Locate every Babesia divergens-infected red blood cell.
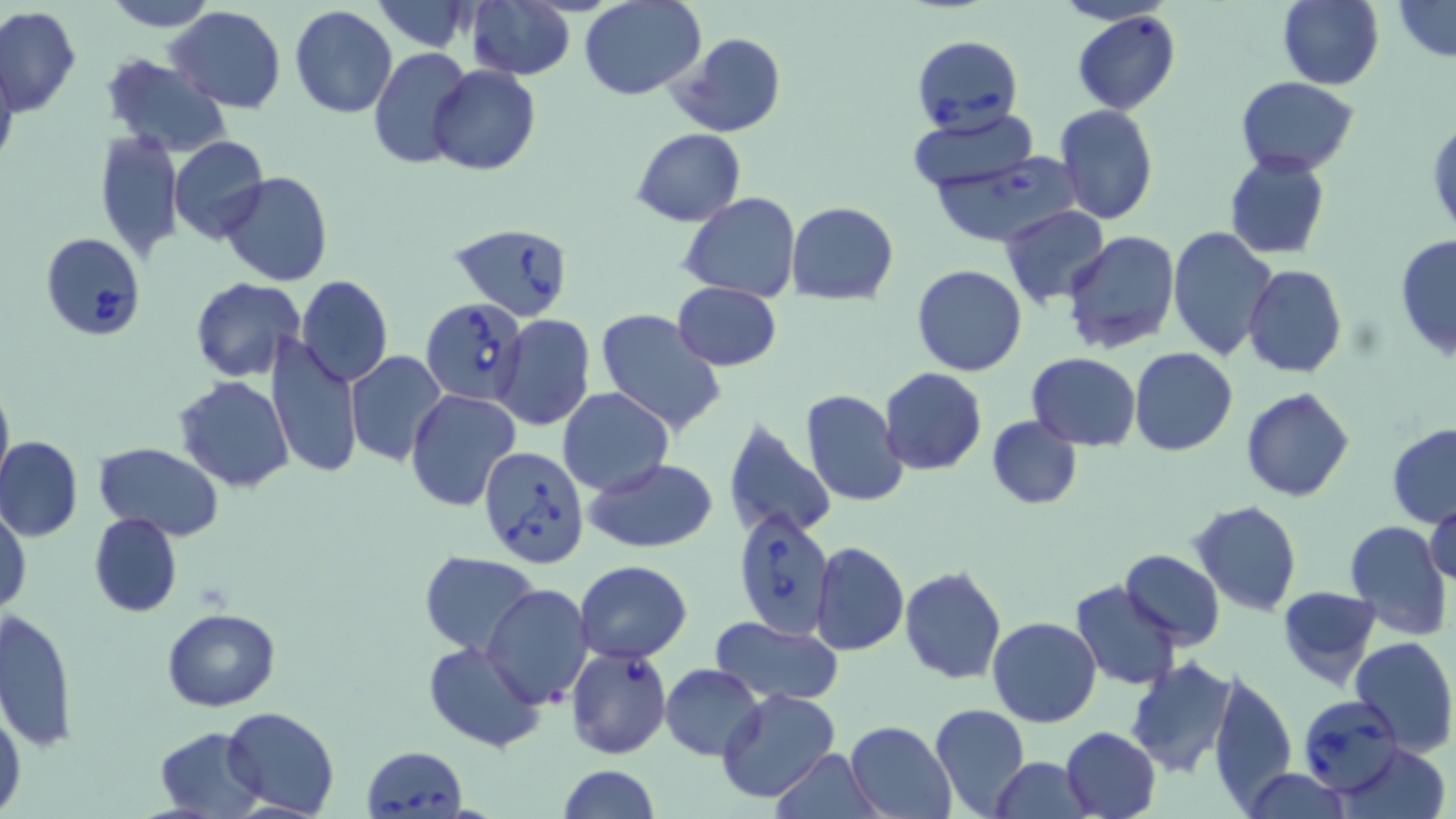

Approximate bounding boxes as (x1,y1)-(x2,y2) corner pairs in pixels.
Babesia divergens-infected red blood cells: (915,35)-(1021,134), (929,151)-(1086,248), (449,228)-(568,320), (42,234)-(148,343), (420,299)-(526,405), (478,445)-(590,569), (729,507)-(838,639), (565,646)-(672,759), (1298,694)-(1402,796), (360,746)-(467,819).

Summary:
  - Uninfected red blood cell locations: (102,0)-(218,31), (1277,0)-(1383,90), (1392,0)-(1456,62), (370,1)-(478,51), (577,1)-(707,101), (468,3)-(575,79), (289,4)-(398,119), (0,5)-(81,116), (168,7)-(287,112), (1071,11)-(1180,115), (665,31)-(789,138), (370,46)-(475,171), (104,54)-(232,157), (0,55)-(20,173), (429,66)-(540,177), (1236,75)-(1359,176), (1054,103)-(1158,224), (909,111)-(1040,191), (1428,119)-(1456,238), (631,128)-(745,226), (95,131)-(183,262), (169,135)-(269,242), (1224,149)-(1331,259), (220,170)-(332,287), (680,193)-(801,302), (785,202)-(899,304), (998,203)-(1111,307), (1169,225)-(1279,362), (1063,230)-(1179,354), (1394,234)-(1456,361), (912,264)-(1027,377), (1243,264)-(1347,380), (297,275)-(393,388), (190,277)-(304,382), (672,281)-(782,370), (596,308)-(728,437), (493,314)-(594,431), (266,334)-(363,482), (1129,346)-(1238,456), (344,351)-(449,467), (1028,351)-(1141,451), (878,367)-(987,476), (175,376)-(293,493), (0,379)-(13,491), (1240,386)-(1356,503), (557,387)-(673,497), (799,389)-(909,506), (407,390)-(522,513), (986,416)-(1081,509), (723,418)-(835,540), (1387,423)-(1456,526), (0,436)-(83,541), (95,442)-(222,541), (583,458)-(718,553), (1426,496)-(1456,592), (1190,501)-(1302,617), (0,506)-(29,618), (89,512)-(184,617), (1343,518)-(1452,639), (810,541)-(908,656), (1119,549)-(1225,647), (420,550)-(540,657), (573,560)-(693,662), (900,565)-(1006,682), (1070,581)-(1182,691), (483,584)-(592,709), (1277,585)-(1382,692), (162,607)-(280,712), (2,608)-(77,750), (708,614)-(845,705), (987,615)-(1102,728), (1349,637)-(1456,756), (423,640)-(547,751), (1126,656)-(1237,776), (661,663)-(766,760), (1209,669)-(1298,812), (716,688)-(839,802), (0,703)-(26,819), (928,703)-(1031,817), (222,705)-(339,818), (845,720)-(957,819), (156,726)-(266,817), (1060,726)-(1161,818), (1333,744)-(1452,819), (773,746)-(880,819), (990,758)-(1095,818), (556,764)-(660,819), (1240,769)-(1351,818)
  - Slide-level diagnosis: Babesia divergens
  - Modality: light microscopy
  - Field of view: single
  - Image size: 1456×819 pixels
  - Stain: May-Grünwald-Giemsa
  - Preparation: thin blood film
  - Magnification: 1000x